Name the cell type shown.
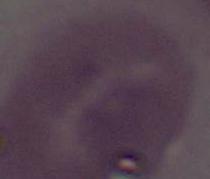

An erythrocyte.

magnification = 1000x
modality = micrograph